Assess this cell for malaria.
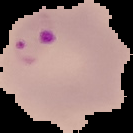
It is parasitized.

From a thin blood film. Cell region segmented out of the field of view; the surrounding area is masked to black. Image is 133×133 pixels.